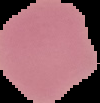

Summary:
  - Image size: 100×103 pixels
  - Result: no malaria parasites detected
  - Image type: segmented cell region on a black background
  - Preparation: thin blood smear